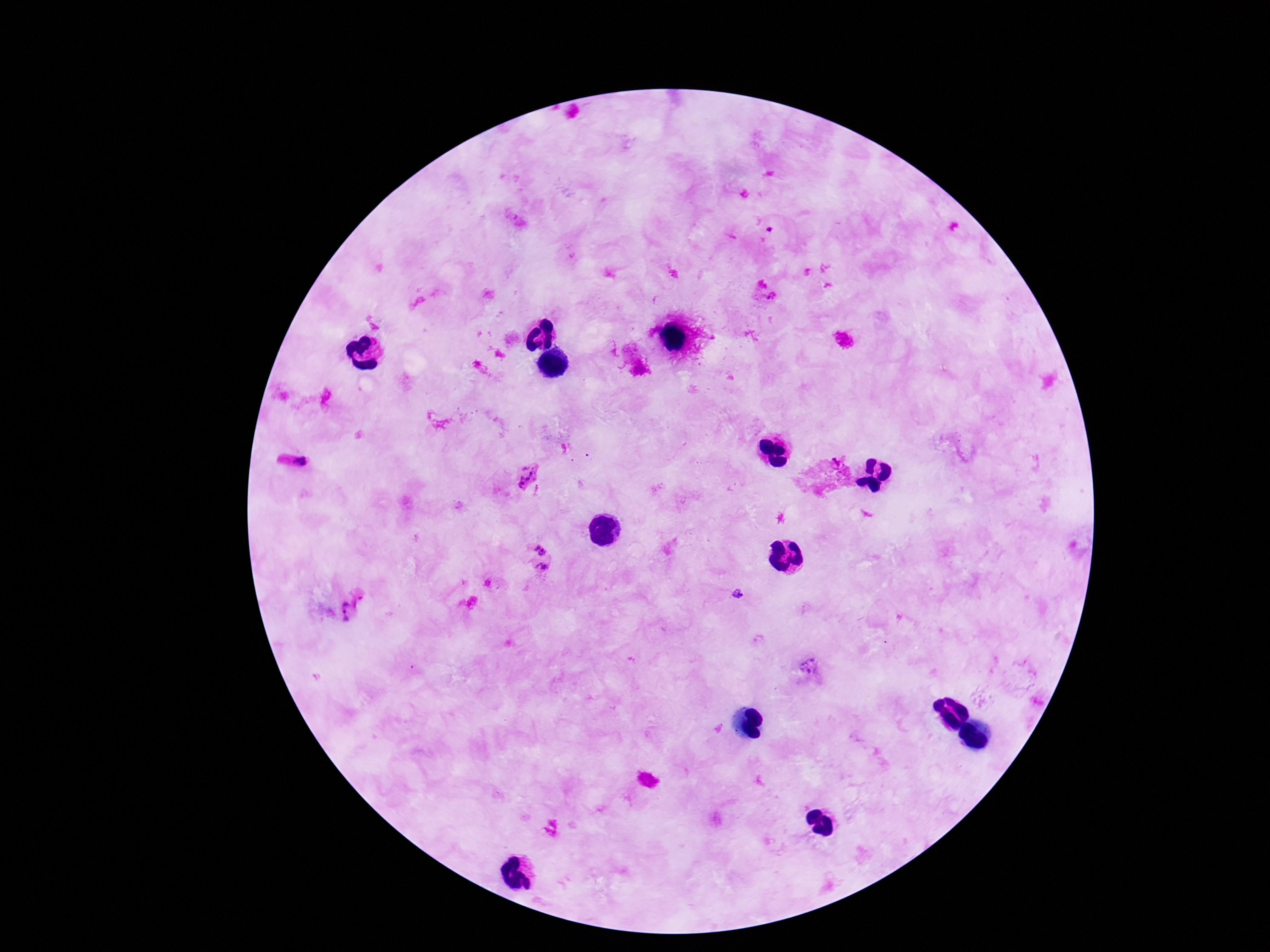

Approximate object centers, in pixels from the top-left corner. Plasmodium parasite locations: (x=294, y=464), (x=527, y=474), (x=539, y=491), (x=540, y=549), (x=544, y=567), (x=361, y=602), (x=344, y=611). Patient malaria status: infected. Giemsa stain. Smartphone photograph taken through the microscope eyepiece. One field from this slide. Image is 1270×952 pixels. 100x magnification. Thick blood smear.